Outline each uninfected red blood cell.
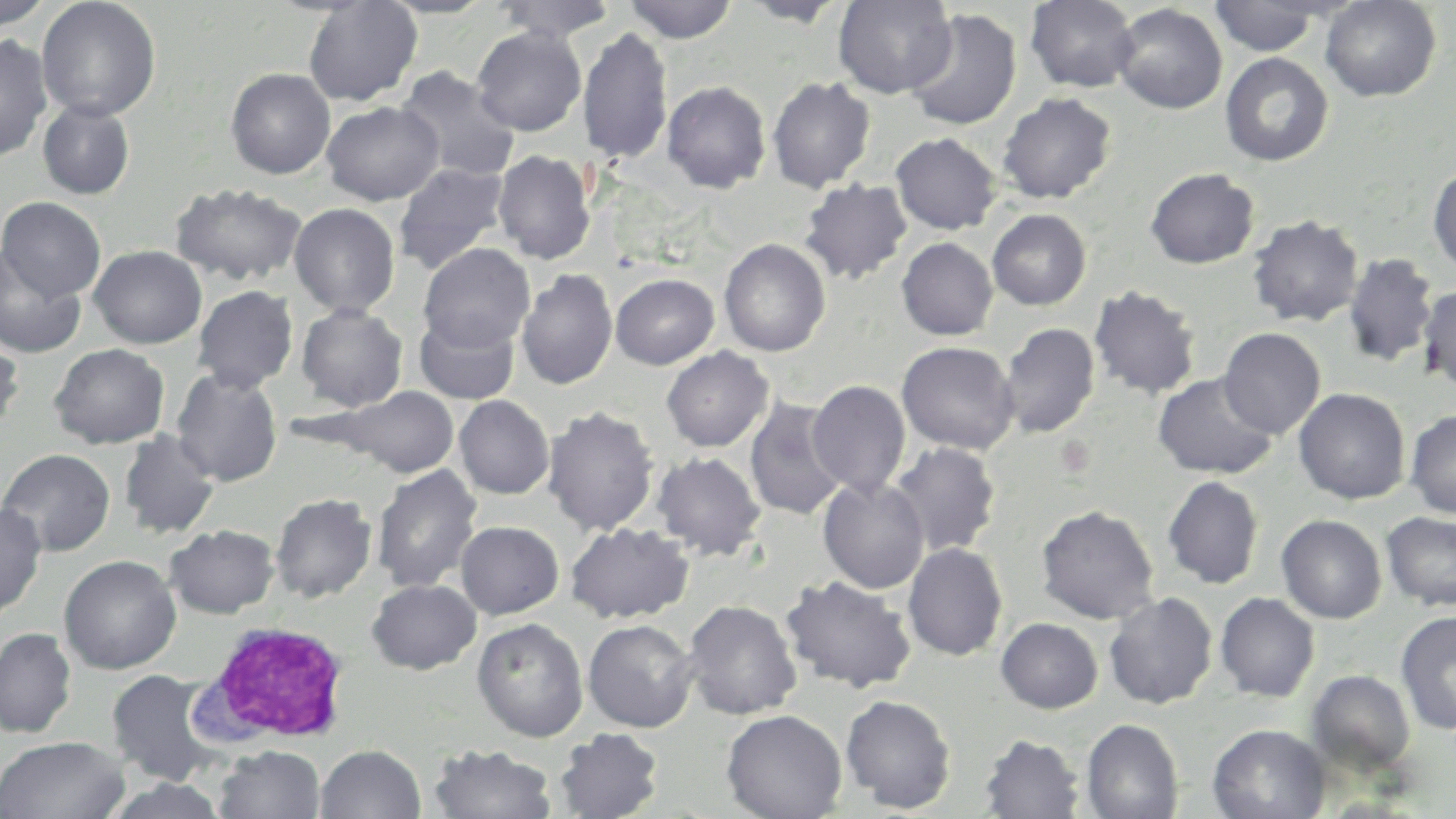

Approximate bounding boxes as named x1/y1/x2/y2 corners in pixels.
Uninfected red blood cells: (x1=36, y1=0, x2=161, y2=121), (x1=303, y1=0, x2=423, y2=106), (x1=624, y1=0, x2=738, y2=43), (x1=833, y1=0, x2=958, y2=98), (x1=1025, y1=0, x2=1140, y2=92), (x1=1320, y1=0, x2=1441, y2=102), (x1=0, y1=1, x2=54, y2=28), (x1=378, y1=1, x2=498, y2=18), (x1=494, y1=1, x2=616, y2=43), (x1=739, y1=1, x2=852, y2=27), (x1=1210, y1=1, x2=1324, y2=56), (x1=1111, y1=3, x2=1228, y2=114), (x1=904, y1=8, x2=1022, y2=132), (x1=471, y1=26, x2=587, y2=135), (x1=578, y1=28, x2=673, y2=165), (x1=0, y1=34, x2=53, y2=162), (x1=1220, y1=52, x2=1334, y2=167), (x1=396, y1=66, x2=520, y2=183), (x1=225, y1=68, x2=336, y2=179), (x1=767, y1=76, x2=876, y2=192), (x1=661, y1=80, x2=771, y2=193), (x1=996, y1=92, x2=1117, y2=204), (x1=37, y1=100, x2=135, y2=199), (x1=321, y1=100, x2=443, y2=205), (x1=890, y1=132, x2=1002, y2=235), (x1=493, y1=149, x2=595, y2=264), (x1=393, y1=162, x2=510, y2=274), (x1=1428, y1=165, x2=1456, y2=274), (x1=1144, y1=167, x2=1260, y2=269), (x1=799, y1=178, x2=913, y2=285), (x1=169, y1=182, x2=307, y2=286), (x1=1, y1=197, x2=106, y2=301), (x1=289, y1=202, x2=400, y2=317), (x1=987, y1=208, x2=1092, y2=310), (x1=1247, y1=215, x2=1364, y2=327), (x1=896, y1=237, x2=998, y2=340), (x1=719, y1=238, x2=831, y2=357), (x1=418, y1=243, x2=535, y2=352), (x1=88, y1=245, x2=207, y2=349), (x1=0, y1=248, x2=86, y2=358), (x1=1343, y1=252, x2=1438, y2=369), (x1=516, y1=268, x2=617, y2=390), (x1=610, y1=273, x2=719, y2=369), (x1=1418, y1=284, x2=1456, y2=391), (x1=192, y1=285, x2=299, y2=392), (x1=1089, y1=285, x2=1202, y2=400), (x1=295, y1=302, x2=409, y2=412), (x1=413, y1=311, x2=521, y2=405), (x1=998, y1=322, x2=1100, y2=438), (x1=1218, y1=327, x2=1326, y2=439), (x1=0, y1=336, x2=24, y2=437), (x1=896, y1=341, x2=1020, y2=454), (x1=49, y1=343, x2=169, y2=449), (x1=661, y1=346, x2=774, y2=452), (x1=171, y1=368, x2=283, y2=487), (x1=1152, y1=373, x2=1279, y2=479), (x1=807, y1=380, x2=911, y2=497), (x1=332, y1=386, x2=460, y2=478), (x1=1294, y1=388, x2=1411, y2=504), (x1=453, y1=395, x2=554, y2=499), (x1=744, y1=396, x2=849, y2=521), (x1=542, y1=405, x2=659, y2=536), (x1=1405, y1=409, x2=1456, y2=519), (x1=119, y1=429, x2=221, y2=539), (x1=887, y1=442, x2=1002, y2=556), (x1=0, y1=448, x2=115, y2=557), (x1=652, y1=451, x2=766, y2=560), (x1=371, y1=465, x2=482, y2=594), (x1=1162, y1=475, x2=1265, y2=589), (x1=817, y1=476, x2=930, y2=593), (x1=270, y1=492, x2=377, y2=603), (x1=0, y1=501, x2=47, y2=621), (x1=1036, y1=505, x2=1159, y2=624), (x1=1382, y1=512, x2=1456, y2=611), (x1=1276, y1=514, x2=1387, y2=623), (x1=455, y1=521, x2=564, y2=619), (x1=565, y1=522, x2=695, y2=624), (x1=165, y1=524, x2=279, y2=618), (x1=902, y1=542, x2=1008, y2=661), (x1=58, y1=554, x2=181, y2=674), (x1=780, y1=575, x2=917, y2=693), (x1=367, y1=579, x2=481, y2=674), (x1=1104, y1=592, x2=1219, y2=709), (x1=1215, y1=592, x2=1320, y2=702), (x1=683, y1=600, x2=802, y2=721), (x1=1396, y1=608, x2=1456, y2=736), (x1=471, y1=617, x2=589, y2=742), (x1=996, y1=617, x2=1103, y2=713), (x1=583, y1=619, x2=699, y2=732), (x1=0, y1=627, x2=77, y2=738), (x1=105, y1=669, x2=224, y2=785), (x1=1307, y1=669, x2=1416, y2=775), (x1=840, y1=694, x2=956, y2=813), (x1=721, y1=709, x2=847, y2=819), (x1=1081, y1=718, x2=1183, y2=819), (x1=1206, y1=724, x2=1330, y2=819), (x1=555, y1=728, x2=664, y2=818), (x1=979, y1=733, x2=1086, y2=818), (x1=0, y1=735, x2=130, y2=819), (x1=428, y1=743, x2=557, y2=819), (x1=215, y1=744, x2=325, y2=819), (x1=315, y1=744, x2=426, y2=818), (x1=101, y1=777, x2=232, y2=819).

{
  "slide_level_diagnosis": "negative for blood parasites",
  "magnification": "1000x",
  "stain": "May-Grünwald-Giemsa",
  "field_of_view": "single",
  "modality": "optical microscopy",
  "image_size": "1456×819 pixels",
  "preparation": "thin blood film",
  "white_blood_cell_locations": "approximate bounding boxes as named x1/y1/x2/y2 corners in pixels: (x1=190, y1=619, x2=354, y2=748)"
}